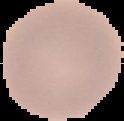

Summary:
  - Image size: 124×121 pixels
  - Malaria status: uninfected
  - Image type: segmented cell region with the area outside set to black
  - Preparation: thin blood smear